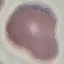 Result: no malaria parasites detected. Giemsa-stained preparation. Cell patch, automatically extracted from a larger field of view and resized to 64 × 64 pixels. Thin blood film. Acquired by smartphone through the microscope eyepiece.